Name the cell type shown.
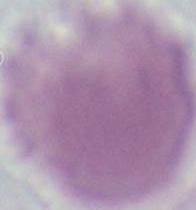

This is an erythrocyte.

Captured at 1000x magnification. Photomicrograph.